Locate every Plasmodium falciparum-infected red blood cell.
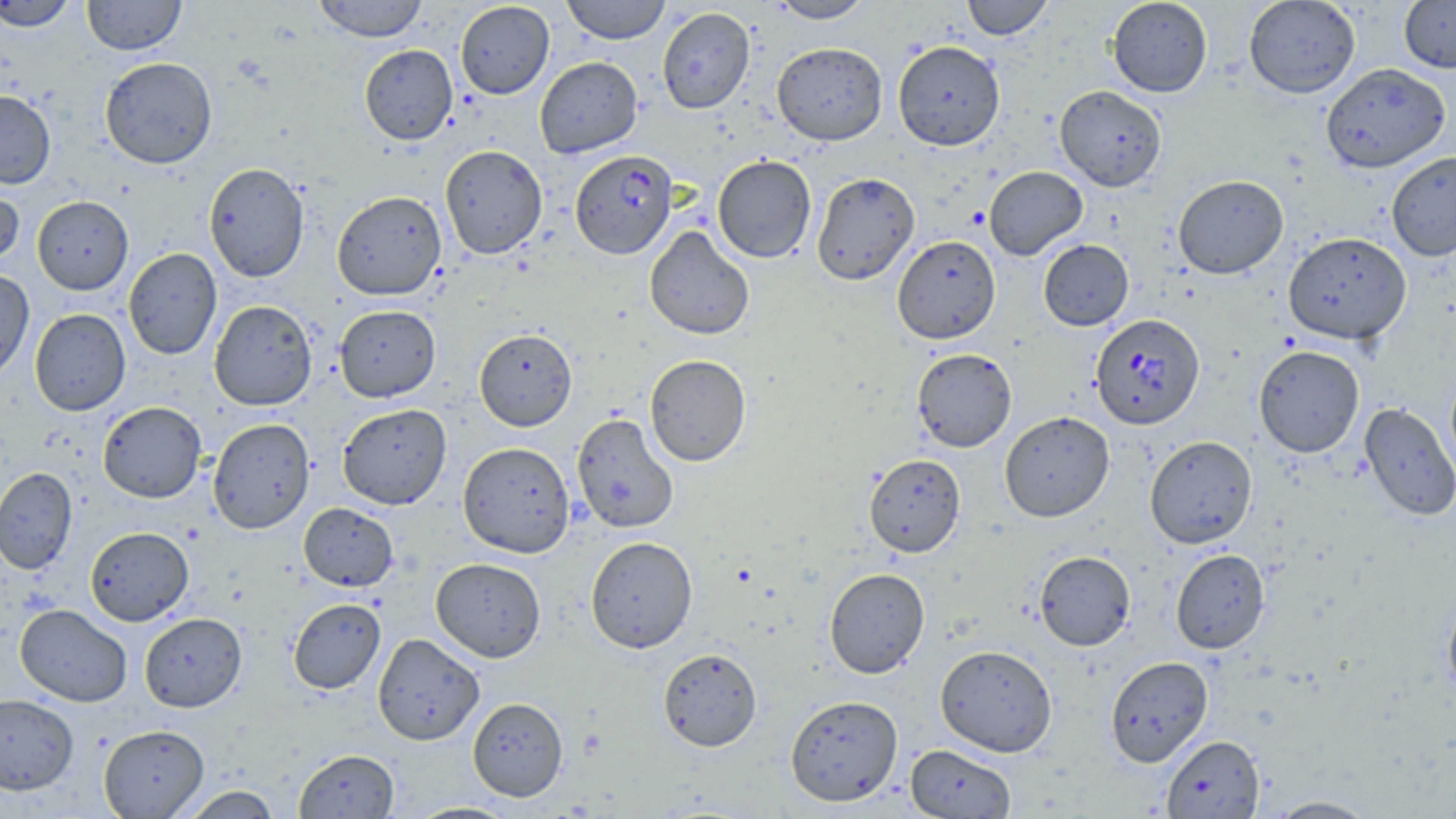

Approximate bounding boxes as (x1,y1)-(x2,y2) corner pairs in pixels.
Plasmodium falciparum-infected red blood cells: (567,150)-(690,258), (1090,313)-(1205,429).

slide-level diagnosis = Plasmodium falciparum
stain = May-Grünwald-Giemsa
modality = optical microscopy
preparation = thin blood smear
magnification = 1000x
uninfected red blood cell locations = approximate bounding boxes as (x1,y1)-(x2,y2) corner pairs in pixels: (1,0)-(79,32), (82,0)-(186,55), (312,0)-(428,42), (561,0)-(672,44), (768,0)-(875,23), (961,0)-(1053,40), (1107,0)-(1213,97), (1244,0)-(1361,98), (1399,0)-(1456,73), (455,2)-(554,99), (657,7)-(755,114), (893,40)-(1005,150), (772,42)-(888,145), (359,44)-(458,145), (535,56)-(642,158), (99,57)-(217,169), (1320,62)-(1450,173), (1054,85)-(1167,191), (0,90)-(56,188), (440,144)-(548,259), (1386,151)-(1456,261), (712,155)-(817,263), (204,162)-(309,282), (984,166)-(1088,260), (811,172)-(920,286), (1172,174)-(1289,279), (0,182)-(24,269), (332,191)-(446,300), (32,196)-(133,295), (644,226)-(755,340), (1283,232)-(1411,345), (892,235)-(1001,344), (1038,239)-(1134,331), (123,248)-(222,360), (0,268)-(34,383), (209,300)-(317,411), (209,303)-(442,405), (334,305)-(441,402), (30,308)-(131,415), (473,328)-(578,431), (1253,345)-(1364,457), (911,348)-(1017,452), (643,354)-(752,467), (1445,366)-(1456,481), (98,401)-(206,503), (1359,401)-(1456,522), (337,403)-(452,510), (1000,411)-(1115,521), (571,412)-(679,533), (208,418)-(315,534), (1145,435)-(1258,548), (458,441)-(575,557), (863,453)-(966,557), (0,467)-(78,575), (298,503)-(398,591), (85,526)-(194,626), (585,536)-(698,653), (1170,548)-(1270,653), (1034,550)-(1136,651), (430,557)-(546,662), (824,567)-(930,678), (1441,585)-(1456,702), (288,598)-(386,694), (15,604)-(132,707), (139,612)-(247,712), (372,633)-(485,745), (935,644)-(1057,757), (657,648)-(762,751), (1105,656)-(1213,766), (0,693)-(79,794), (785,695)-(903,806), (467,697)-(568,801), (99,724)-(209,818), (1161,734)-(1266,818), (905,744)-(1016,818), (293,748)-(399,818), (179,786)-(282,818), (1263,796)-(1381,818), (405,802)-(520,819)
field of view = one of a larger specimen
image size = 1456×819 pixels